Give the extent of all Plasmodium falciparum-infected red blood cells.
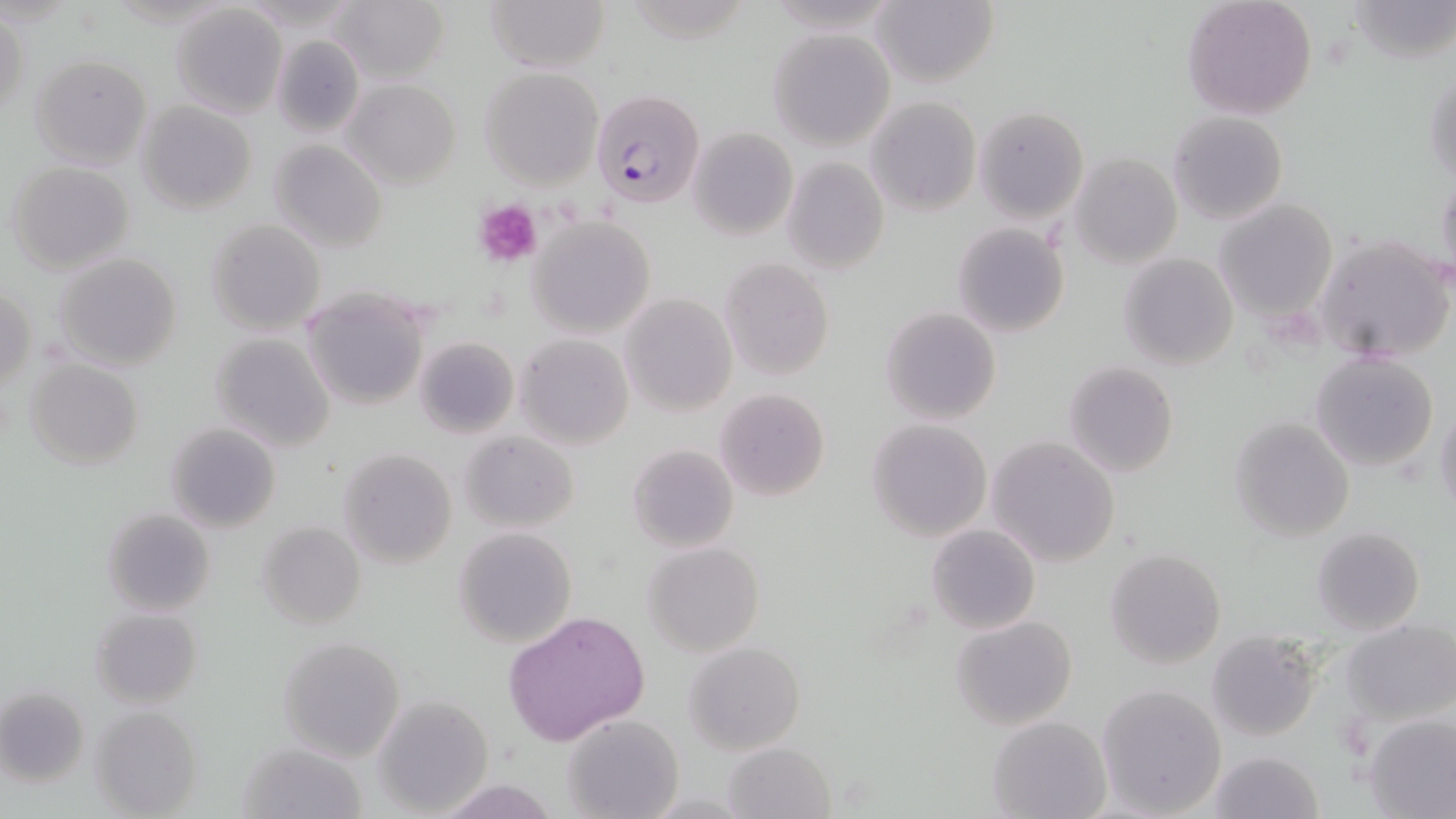

Approximate bounding boxes as named x1/y1/x2/y2 corners in pixels.
Plasmodium falciparum-infected red blood cells: (x1=590, y1=89, x2=707, y2=210).

Summary:
  - Platelet locations: (x1=473, y1=198, x2=544, y2=269)
  - Uninfected red blood cell locations: (x1=329, y1=0, x2=448, y2=85), (x1=484, y1=0, x2=611, y2=73), (x1=871, y1=0, x2=999, y2=90), (x1=1181, y1=0, x2=1318, y2=119), (x1=1347, y1=0, x2=1454, y2=65), (x1=170, y1=3, x2=287, y2=117), (x1=0, y1=11, x2=27, y2=124), (x1=768, y1=29, x2=894, y2=149), (x1=272, y1=35, x2=365, y2=138), (x1=31, y1=54, x2=153, y2=170), (x1=1424, y1=63, x2=1456, y2=189), (x1=479, y1=68, x2=603, y2=189), (x1=342, y1=78, x2=461, y2=189), (x1=866, y1=95, x2=981, y2=216), (x1=136, y1=100, x2=257, y2=215), (x1=974, y1=105, x2=1088, y2=225), (x1=1167, y1=111, x2=1288, y2=224), (x1=688, y1=126, x2=797, y2=240), (x1=268, y1=139, x2=388, y2=253), (x1=1069, y1=153, x2=1183, y2=267), (x1=781, y1=156, x2=889, y2=275), (x1=5, y1=161, x2=136, y2=276), (x1=1435, y1=169, x2=1456, y2=284), (x1=1216, y1=198, x2=1338, y2=322), (x1=527, y1=215, x2=656, y2=336), (x1=206, y1=219, x2=325, y2=337), (x1=952, y1=222, x2=1070, y2=337), (x1=1315, y1=233, x2=1455, y2=364), (x1=54, y1=252, x2=182, y2=372), (x1=1119, y1=253, x2=1239, y2=370), (x1=718, y1=258, x2=834, y2=382), (x1=1, y1=285, x2=36, y2=395), (x1=301, y1=288, x2=431, y2=410), (x1=620, y1=292, x2=737, y2=416), (x1=880, y1=307, x2=1002, y2=424), (x1=209, y1=332, x2=334, y2=452), (x1=514, y1=333, x2=634, y2=450), (x1=414, y1=336, x2=518, y2=438), (x1=1308, y1=352, x2=1439, y2=473), (x1=25, y1=358, x2=144, y2=471), (x1=1063, y1=361, x2=1178, y2=477), (x1=715, y1=388, x2=831, y2=501), (x1=1435, y1=398, x2=1456, y2=526), (x1=1228, y1=417, x2=1355, y2=541), (x1=866, y1=419, x2=992, y2=541), (x1=166, y1=423, x2=281, y2=533), (x1=460, y1=430, x2=579, y2=532), (x1=985, y1=436, x2=1121, y2=567), (x1=627, y1=443, x2=739, y2=553), (x1=337, y1=448, x2=458, y2=570), (x1=102, y1=507, x2=216, y2=616), (x1=258, y1=521, x2=366, y2=630), (x1=926, y1=523, x2=1041, y2=635), (x1=1312, y1=526, x2=1425, y2=637), (x1=453, y1=528, x2=577, y2=647), (x1=643, y1=542, x2=764, y2=656), (x1=1104, y1=548, x2=1227, y2=669), (x1=91, y1=608, x2=202, y2=710), (x1=503, y1=609, x2=650, y2=744), (x1=951, y1=616, x2=1078, y2=730), (x1=1342, y1=619, x2=1456, y2=724), (x1=1204, y1=633, x2=1320, y2=742), (x1=277, y1=636, x2=405, y2=762), (x1=684, y1=642, x2=806, y2=754), (x1=1094, y1=683, x2=1228, y2=817), (x1=0, y1=687, x2=89, y2=787), (x1=370, y1=694, x2=494, y2=816), (x1=88, y1=705, x2=204, y2=818), (x1=1363, y1=713, x2=1456, y2=818), (x1=562, y1=714, x2=683, y2=819), (x1=986, y1=715, x2=1111, y2=819), (x1=238, y1=741, x2=369, y2=819), (x1=725, y1=742, x2=835, y2=818), (x1=1207, y1=750, x2=1322, y2=819)
  - Slide-level diagnosis: Plasmodium falciparum
  - Field of view: single
  - Modality: optical microscopy
  - Image size: 1456×819 pixels
  - Preparation: thin blood smear
  - Magnification: 1000x
  - Stain: May-Grünwald-Giemsa